Locate and identify every blood parasite.
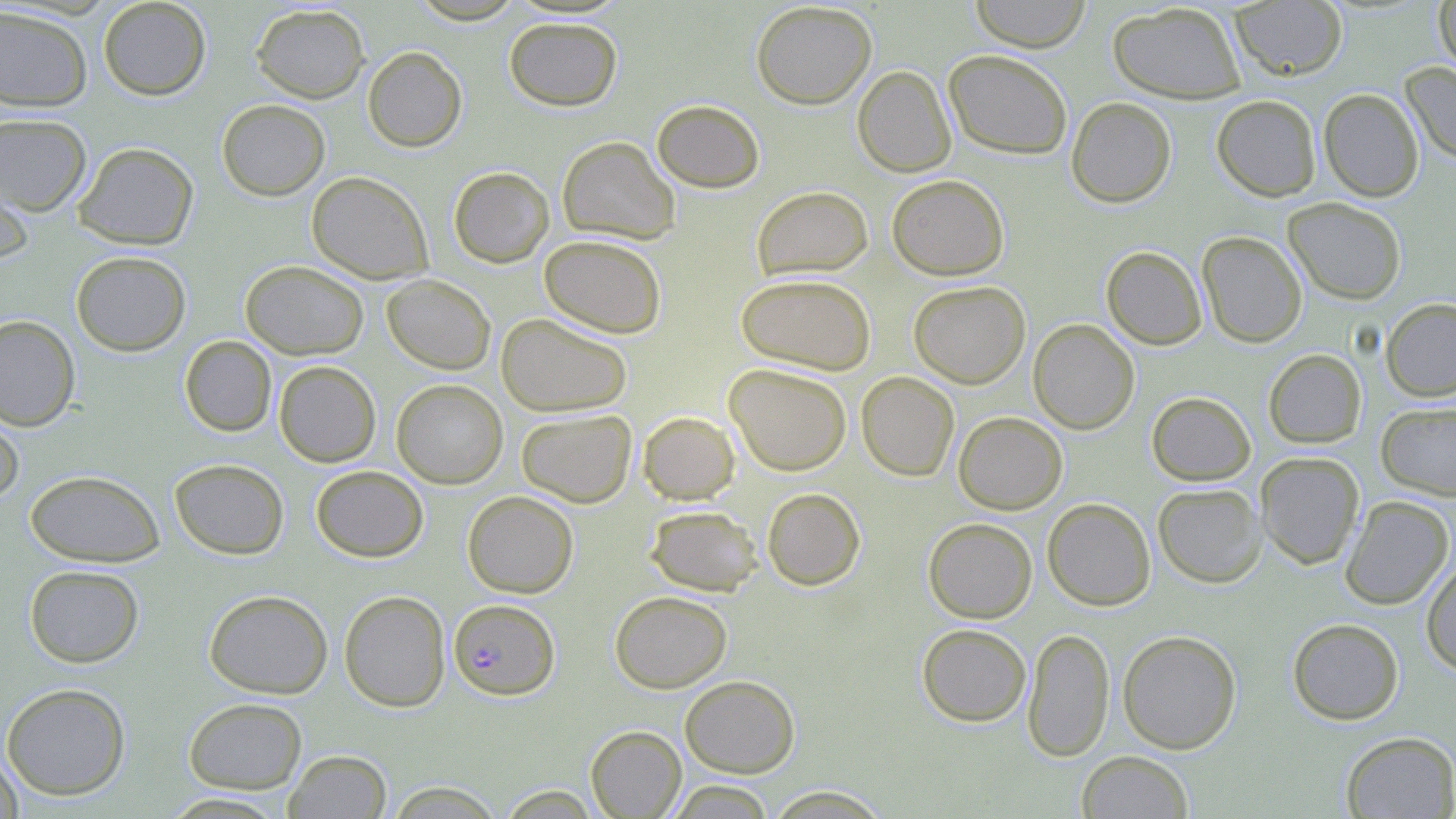

Approximate bounding boxes as (x1,y1)-(x2,y2) corner pairs in pixels.
Plasmodium falciparum-infected red blood cells: (450,601)-(561,702).
No Plasmodium ovale, Plasmodium malariae, Plasmodium vivax, Babesia divergens, or Trypanosoma brucei observed.

Summary:
  - Uninfected red blood cell locations: (97,0)-(211,101), (409,0)-(527,24), (969,0)-(1091,53), (1230,0)-(1348,81), (1433,0)-(1456,73), (751,2)-(877,110), (1107,2)-(1247,103), (250,3)-(370,104), (0,5)-(93,112), (503,17)-(623,111), (362,46)-(467,152), (943,49)-(1073,160), (1401,62)-(1456,165), (853,66)-(956,177), (1318,88)-(1424,201), (1211,95)-(1321,202), (1066,97)-(1177,208), (216,99)-(331,201), (652,99)-(764,193), (0,113)-(92,216), (557,136)-(680,244), (73,141)-(198,250), (0,156)-(35,267), (448,166)-(554,268), (306,171)-(433,284), (887,174)-(1009,280), (752,185)-(873,281), (1283,198)-(1406,305), (1197,231)-(1307,348), (539,234)-(667,338), (1101,246)-(1207,350), (70,250)-(191,356), (240,260)-(369,360), (736,273)-(876,375), (382,274)-(495,374), (908,281)-(1030,388), (1380,298)-(1456,402), (496,312)-(632,417), (0,314)-(80,430), (1028,318)-(1140,434), (179,336)-(277,437), (1263,349)-(1366,449), (274,361)-(381,467), (724,363)-(852,476), (856,371)-(959,481), (392,379)-(507,489), (1146,391)-(1256,485), (1376,402)-(1456,500), (0,404)-(24,507), (516,409)-(637,508), (638,411)-(740,504), (953,412)-(1067,514), (1255,452)-(1364,569), (170,458)-(289,559), (311,465)-(428,562), (25,469)-(164,567), (1153,483)-(1266,588), (762,487)-(866,590), (462,490)-(579,597), (1340,495)-(1454,610), (1042,498)-(1156,611), (645,505)-(763,596), (923,517)-(1037,623), (1421,560)-(1456,674), (24,565)-(144,668), (204,589)-(333,698), (338,590)-(450,712), (610,591)-(732,693), (1287,617)-(1404,725), (916,623)-(1032,726), (1023,628)-(1114,763), (1117,629)-(1242,754), (680,675)-(800,778), (1,682)-(131,800), (183,697)-(307,794), (586,725)-(686,818), (1340,731)-(1456,818), (0,750)-(24,819), (284,750)-(391,818), (1077,751)-(1193,819), (666,780)-(776,818), (385,781)-(505,818), (496,785)-(601,818), (765,786)-(891,818), (160,792)-(289,817)
  - Slide-level diagnosis: Plasmodium falciparum
  - Preparation: thin blood film
  - Image size: 1456×819 pixels
  - Field of view: one of a larger specimen
  - Stain: May-Grünwald-Giemsa
  - Modality: light microscopy
  - Magnification: 1000x